Locate every blood parasite and identify its species.
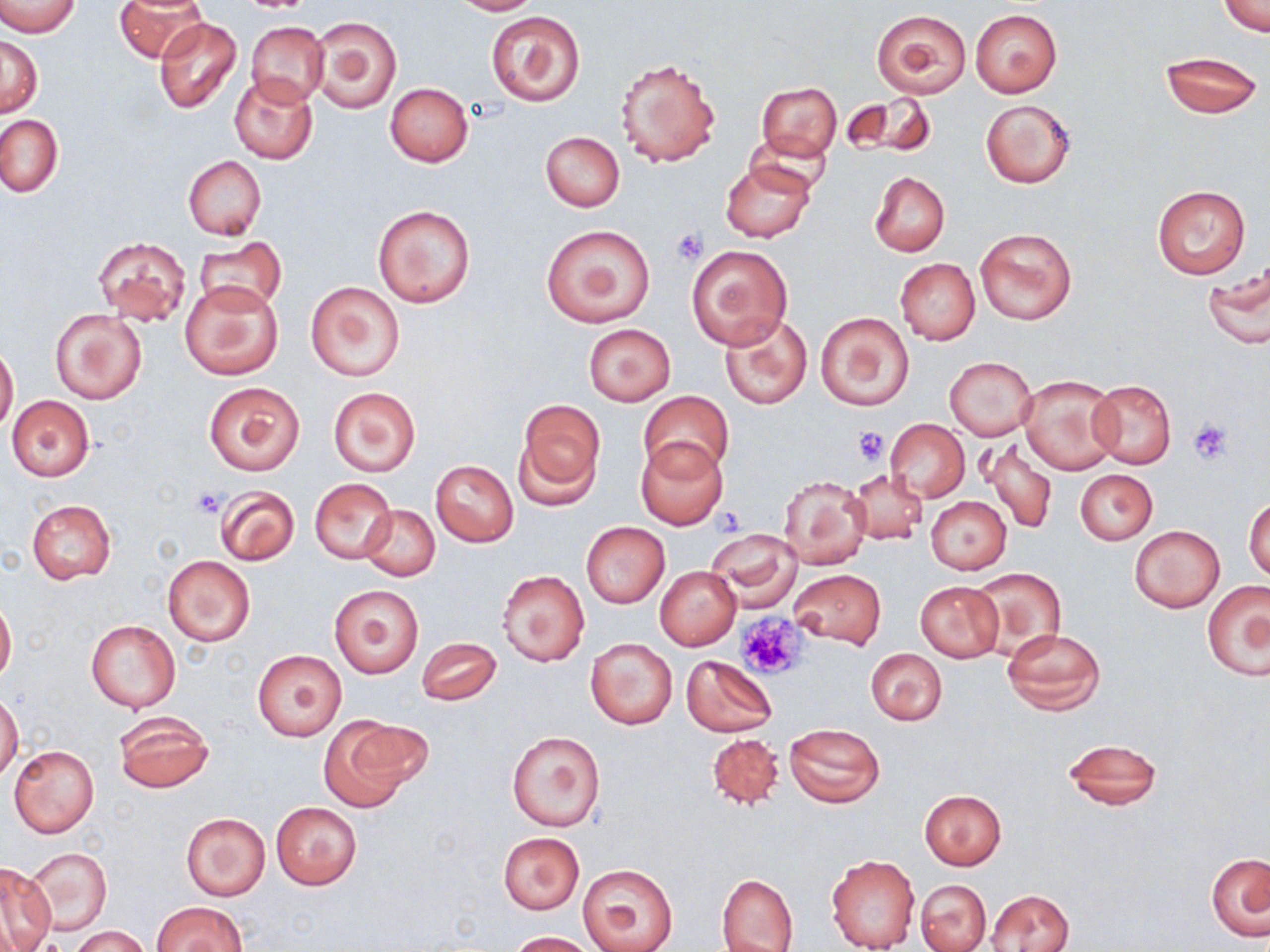

No blood parasites seen.

Approximate bounding boxes as named x1/y1/x2/y2 corners in pixels. Uninfected red blood cell locations: (x1=116, y1=0, x2=208, y2=63), (x1=450, y1=0, x2=542, y2=15), (x1=1221, y1=0, x2=1268, y2=37), (x1=1, y1=1, x2=80, y2=36), (x1=870, y1=8, x2=972, y2=98), (x1=970, y1=9, x2=1062, y2=97), (x1=486, y1=11, x2=585, y2=107), (x1=309, y1=16, x2=402, y2=113), (x1=153, y1=17, x2=242, y2=115), (x1=246, y1=21, x2=329, y2=105), (x1=1, y1=36, x2=42, y2=116), (x1=1159, y1=50, x2=1264, y2=119), (x1=615, y1=58, x2=720, y2=167), (x1=229, y1=74, x2=319, y2=164), (x1=385, y1=83, x2=473, y2=167), (x1=756, y1=83, x2=841, y2=162), (x1=844, y1=93, x2=936, y2=159), (x1=981, y1=100, x2=1075, y2=188), (x1=1, y1=115, x2=63, y2=197), (x1=750, y1=125, x2=834, y2=195), (x1=541, y1=131, x2=625, y2=211), (x1=183, y1=155, x2=266, y2=239), (x1=720, y1=160, x2=815, y2=243), (x1=871, y1=171, x2=949, y2=256), (x1=1152, y1=184, x2=1252, y2=280), (x1=373, y1=204, x2=475, y2=307), (x1=539, y1=223, x2=655, y2=328), (x1=974, y1=226, x2=1076, y2=325), (x1=93, y1=236, x2=191, y2=326), (x1=194, y1=236, x2=286, y2=314), (x1=686, y1=245, x2=793, y2=349), (x1=895, y1=258, x2=980, y2=345), (x1=1204, y1=265, x2=1270, y2=350), (x1=180, y1=279, x2=283, y2=379), (x1=306, y1=281, x2=407, y2=380), (x1=51, y1=307, x2=147, y2=405), (x1=815, y1=311, x2=915, y2=411), (x1=719, y1=312, x2=812, y2=410), (x1=583, y1=324, x2=675, y2=405), (x1=0, y1=343, x2=18, y2=435), (x1=944, y1=356, x2=1038, y2=441), (x1=1018, y1=375, x2=1122, y2=475), (x1=1088, y1=379, x2=1177, y2=469), (x1=204, y1=381, x2=304, y2=475), (x1=327, y1=387, x2=420, y2=476), (x1=640, y1=391, x2=732, y2=480), (x1=6, y1=395, x2=95, y2=481), (x1=516, y1=400, x2=604, y2=505), (x1=884, y1=418, x2=969, y2=503), (x1=981, y1=435, x2=1057, y2=536), (x1=634, y1=437, x2=729, y2=530), (x1=430, y1=460, x2=519, y2=547), (x1=847, y1=469, x2=929, y2=545), (x1=1076, y1=469, x2=1156, y2=544), (x1=779, y1=474, x2=872, y2=570), (x1=310, y1=479, x2=396, y2=563), (x1=213, y1=485, x2=299, y2=566), (x1=1245, y1=494, x2=1270, y2=581), (x1=926, y1=496, x2=1011, y2=573), (x1=26, y1=499, x2=116, y2=584), (x1=361, y1=503, x2=439, y2=579), (x1=581, y1=522, x2=669, y2=608), (x1=1131, y1=525, x2=1224, y2=611), (x1=707, y1=531, x2=798, y2=606), (x1=163, y1=556, x2=256, y2=646), (x1=970, y1=566, x2=1066, y2=657), (x1=655, y1=567, x2=741, y2=651), (x1=788, y1=569, x2=885, y2=647), (x1=498, y1=570, x2=589, y2=667), (x1=915, y1=582, x2=1004, y2=661), (x1=1203, y1=582, x2=1270, y2=681), (x1=329, y1=584, x2=424, y2=679), (x1=0, y1=598, x2=16, y2=682), (x1=85, y1=619, x2=181, y2=713), (x1=1001, y1=627, x2=1106, y2=715), (x1=416, y1=636, x2=502, y2=706), (x1=586, y1=638, x2=676, y2=730), (x1=865, y1=649, x2=947, y2=725), (x1=253, y1=650, x2=346, y2=740), (x1=681, y1=655, x2=777, y2=737), (x1=0, y1=693, x2=23, y2=781), (x1=112, y1=711, x2=215, y2=794), (x1=318, y1=716, x2=417, y2=809), (x1=784, y1=723, x2=885, y2=807), (x1=507, y1=730, x2=606, y2=831), (x1=707, y1=732, x2=785, y2=810), (x1=1062, y1=738, x2=1163, y2=811), (x1=8, y1=745, x2=99, y2=838), (x1=919, y1=789, x2=1007, y2=869), (x1=271, y1=803, x2=361, y2=890), (x1=182, y1=813, x2=270, y2=900), (x1=498, y1=833, x2=584, y2=913), (x1=28, y1=847, x2=111, y2=935), (x1=1208, y1=851, x2=1270, y2=942), (x1=826, y1=852, x2=920, y2=951), (x1=1, y1=861, x2=56, y2=949), (x1=576, y1=863, x2=677, y2=952), (x1=716, y1=874, x2=799, y2=952), (x1=915, y1=878, x2=991, y2=951), (x1=989, y1=889, x2=1074, y2=952), (x1=153, y1=901, x2=245, y2=951), (x1=71, y1=926, x2=152, y2=952), (x1=507, y1=930, x2=595, y2=951). Platelet locations: (x1=670, y1=227, x2=708, y2=265), (x1=1189, y1=419, x2=1232, y2=463), (x1=850, y1=425, x2=890, y2=464), (x1=192, y1=489, x2=225, y2=517), (x1=713, y1=507, x2=747, y2=539), (x1=734, y1=612, x2=807, y2=680). Slide-level diagnosis: no evidence of blood parasites. May-Grünwald-Giemsa-stained preparation. Thin blood film. Image is 1270×952 pixels. Captured at 1000x magnification. Light microscopy. One field of a larger specimen.